Identify the parasite.
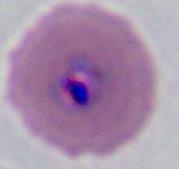

This is Plasmodium.

Captured at either 400x or 1000x magnification. Photomicrograph.